Assess this cell for malaria.
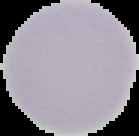
Uninfected.

Image is 139×136 pixels. From a thin blood smear. Cell region segmented out of the field of view; the surrounding area is masked to black.